Comment on the morphology of the erythrocytes.
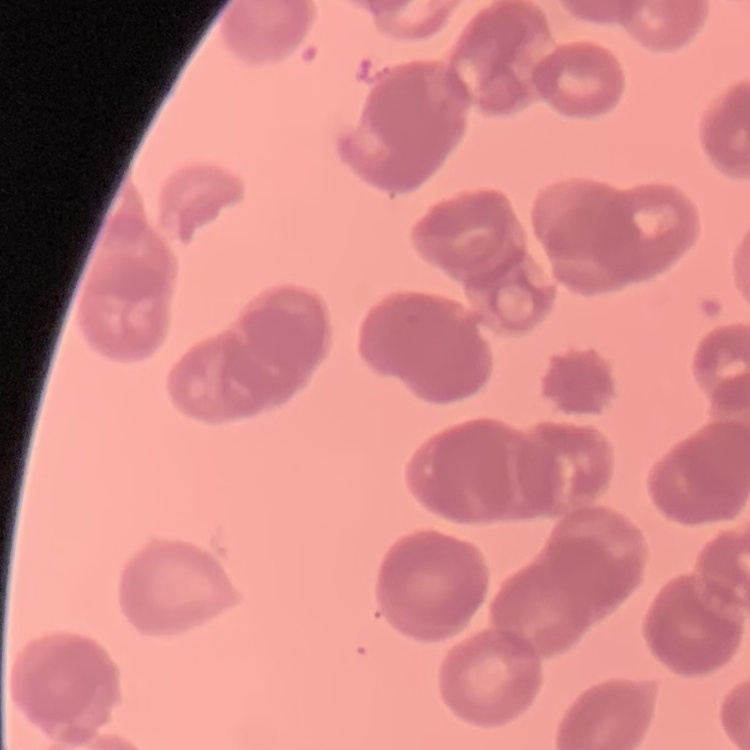

Rouleaux formation.

Summary:
  - Stain: Field's or Giemsa
  - Preparation: thin blood film
  - Image type: one tile cut from a larger photomicrograph